State which cell type is depicted.
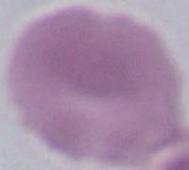
An erythrocyte.

Captured at 1000x magnification. Photomicrograph.